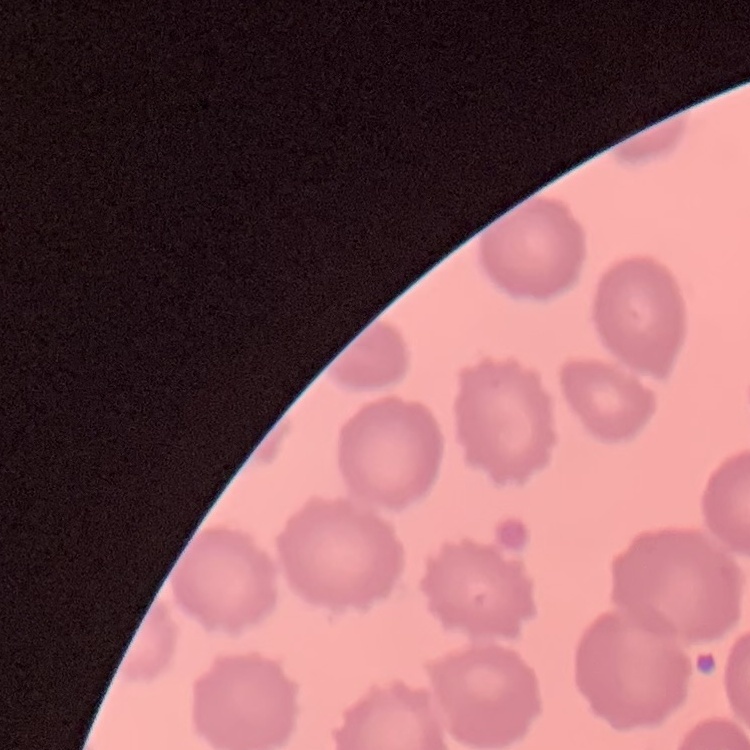

Summary:
  - Red blood cell morphology: no rouleaux formation
  - Stain: Field's or Giemsa
  - Image type: one tile cut from a larger photomicrograph
  - Preparation: thin peripheral smear